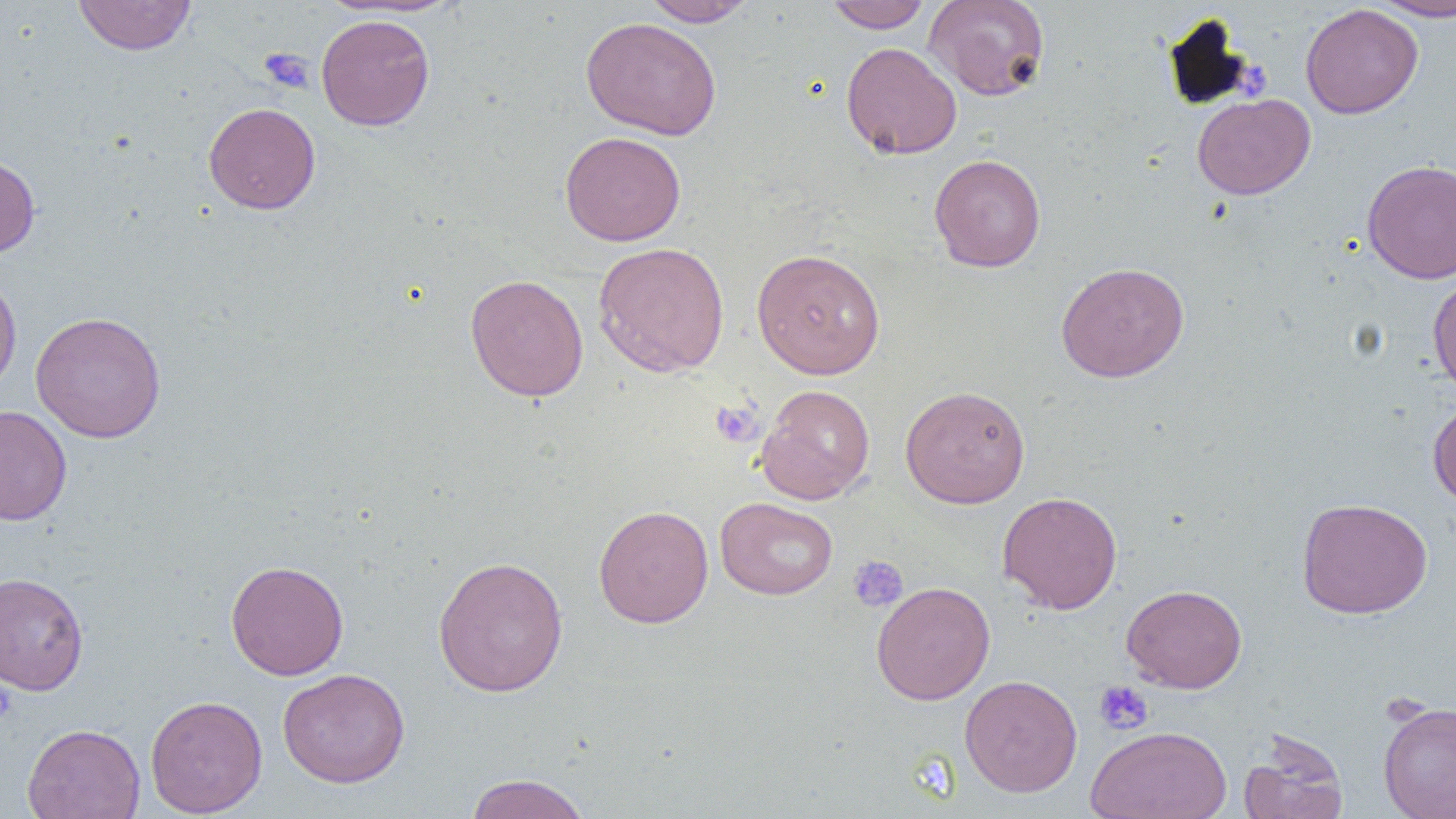
Summary:
  - Coordinate format: approximate bounding boxes as named x1/y1/x2/y2 corners in pixels
  - Platelet locations: (x1=260, y1=48, x2=315, y2=95), (x1=711, y1=399, x2=763, y2=447), (x1=847, y1=555, x2=908, y2=612), (x1=0, y1=680, x2=16, y2=723), (x1=1094, y1=681, x2=1153, y2=735)
  - Uninfected red blood cell locations: (x1=72, y1=0, x2=197, y2=56), (x1=640, y1=0, x2=758, y2=27), (x1=824, y1=0, x2=931, y2=32), (x1=923, y1=0, x2=1051, y2=101), (x1=1368, y1=0, x2=1456, y2=20), (x1=1300, y1=4, x2=1423, y2=118), (x1=316, y1=13, x2=435, y2=131), (x1=581, y1=17, x2=721, y2=140), (x1=841, y1=42, x2=961, y2=159), (x1=1192, y1=93, x2=1315, y2=200), (x1=204, y1=102, x2=321, y2=214), (x1=559, y1=131, x2=686, y2=246), (x1=929, y1=154, x2=1046, y2=272), (x1=0, y1=155, x2=40, y2=258), (x1=1362, y1=159, x2=1456, y2=284), (x1=592, y1=242, x2=730, y2=377), (x1=751, y1=248, x2=886, y2=379), (x1=1056, y1=261, x2=1189, y2=382), (x1=0, y1=268, x2=22, y2=396), (x1=1427, y1=272, x2=1456, y2=396), (x1=465, y1=274, x2=589, y2=401), (x1=31, y1=311, x2=166, y2=443), (x1=756, y1=384, x2=875, y2=505), (x1=900, y1=385, x2=1031, y2=507), (x1=1427, y1=399, x2=1456, y2=507), (x1=0, y1=405, x2=72, y2=526), (x1=997, y1=491, x2=1123, y2=614), (x1=715, y1=497, x2=838, y2=600), (x1=1296, y1=497, x2=1433, y2=618), (x1=593, y1=505, x2=713, y2=628), (x1=432, y1=555, x2=568, y2=697), (x1=225, y1=560, x2=349, y2=680), (x1=0, y1=571, x2=89, y2=696), (x1=870, y1=581, x2=995, y2=705), (x1=1121, y1=584, x2=1247, y2=693), (x1=277, y1=668, x2=410, y2=788), (x1=960, y1=675, x2=1083, y2=797), (x1=144, y1=695, x2=268, y2=817), (x1=1378, y1=700, x2=1456, y2=819), (x1=22, y1=723, x2=145, y2=819), (x1=1086, y1=726, x2=1232, y2=819), (x1=1239, y1=731, x2=1349, y2=819), (x1=464, y1=772, x2=591, y2=819)
  - Slide-level diagnosis: no evidence of blood parasites
  - Magnification: 1000x
  - Preparation: thin blood film
  - Modality: optical microscopy
  - Image size: 1456×819 pixels
  - Field of view: single